Outline platelets.
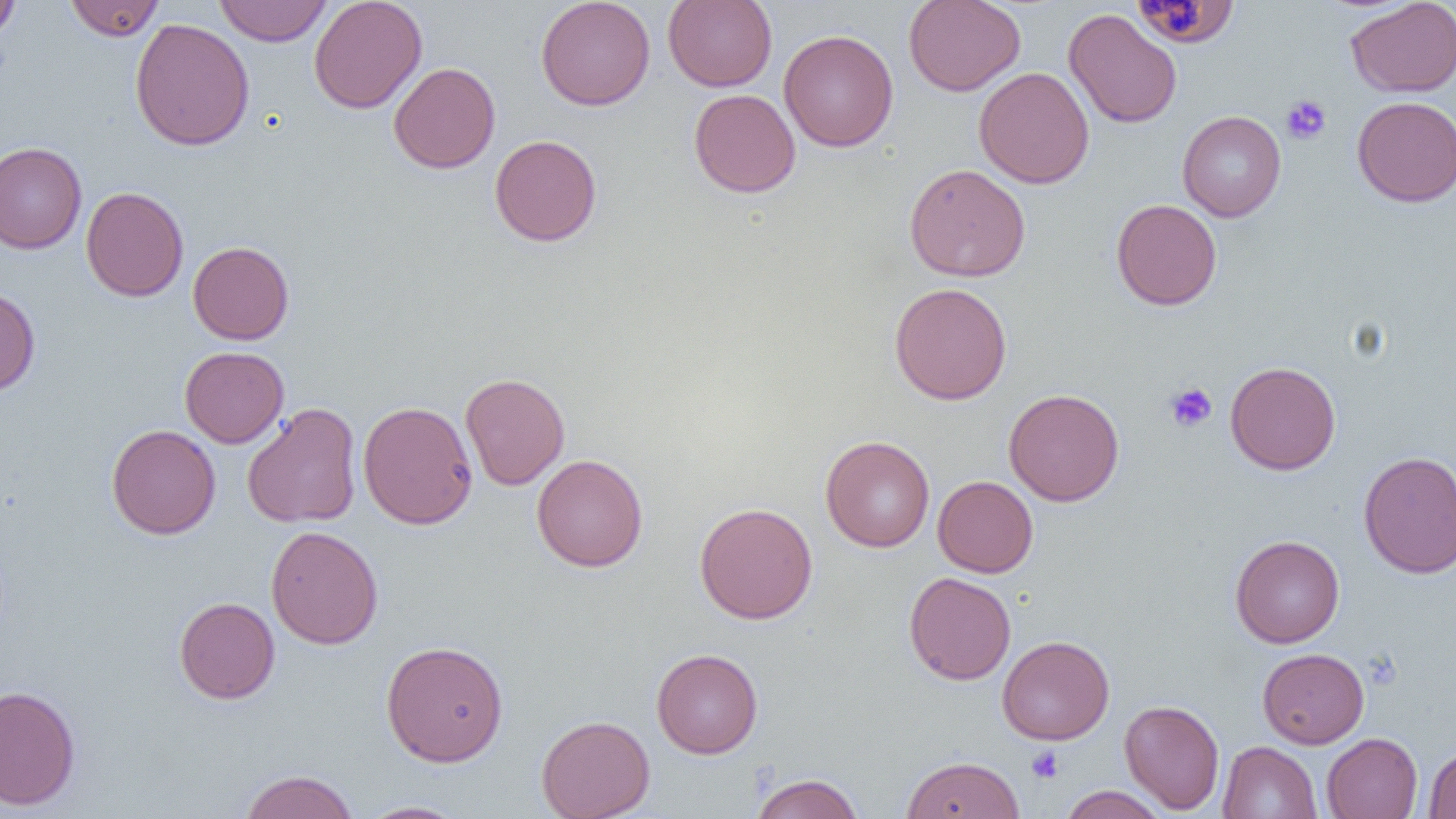

Approximate bounding boxes as (x1, y1, x2, y2) in pixels.
Platelets: (1280, 95, 1332, 144), (1164, 382, 1217, 433), (1026, 746, 1064, 783).

Summary:
  - Uninfected red blood cell locations: (0, 0, 21, 41), (65, 0, 164, 41), (214, 0, 332, 46), (309, 0, 427, 113), (535, 0, 656, 111), (663, 0, 777, 91), (903, 0, 1025, 96), (1345, 0, 1456, 97), (1133, 1, 1237, 48), (1063, 9, 1182, 129), (129, 18, 255, 151), (779, 29, 899, 152), (389, 62, 500, 173), (974, 67, 1094, 189), (689, 89, 801, 197), (1352, 96, 1456, 207), (1177, 110, 1286, 222), (489, 134, 602, 246), (0, 142, 87, 254), (904, 163, 1031, 282), (81, 187, 188, 301), (1111, 199, 1222, 310), (188, 241, 294, 345), (889, 282, 1012, 405), (0, 286, 41, 398), (179, 346, 289, 447), (1225, 360, 1340, 475), (460, 372, 570, 490), (1003, 388, 1124, 506), (357, 400, 478, 529), (242, 403, 362, 528), (259, 403, 372, 649), (106, 424, 221, 539), (820, 435, 935, 552), (1358, 450, 1456, 578), (532, 454, 648, 572), (933, 475, 1038, 577), (694, 502, 818, 624), (266, 525, 384, 650), (1230, 534, 1345, 648), (904, 572, 1016, 685), (174, 597, 280, 704), (997, 635, 1114, 745), (381, 640, 509, 765), (651, 648, 763, 759), (1257, 648, 1369, 748), (0, 685, 82, 811), (1119, 699, 1224, 814), (536, 714, 655, 819), (1321, 733, 1422, 819), (1218, 741, 1321, 819), (1423, 744, 1456, 818), (902, 754, 1024, 818), (239, 769, 359, 819), (750, 773, 865, 819), (1058, 785, 1169, 819), (358, 800, 468, 818)
  - Slide-level diagnosis: no evidence of blood parasites
  - Image size: 1456×819 pixels
  - Magnification: 1000x
  - Field of view: single
  - Preparation: thin blood film
  - Modality: light microscopy